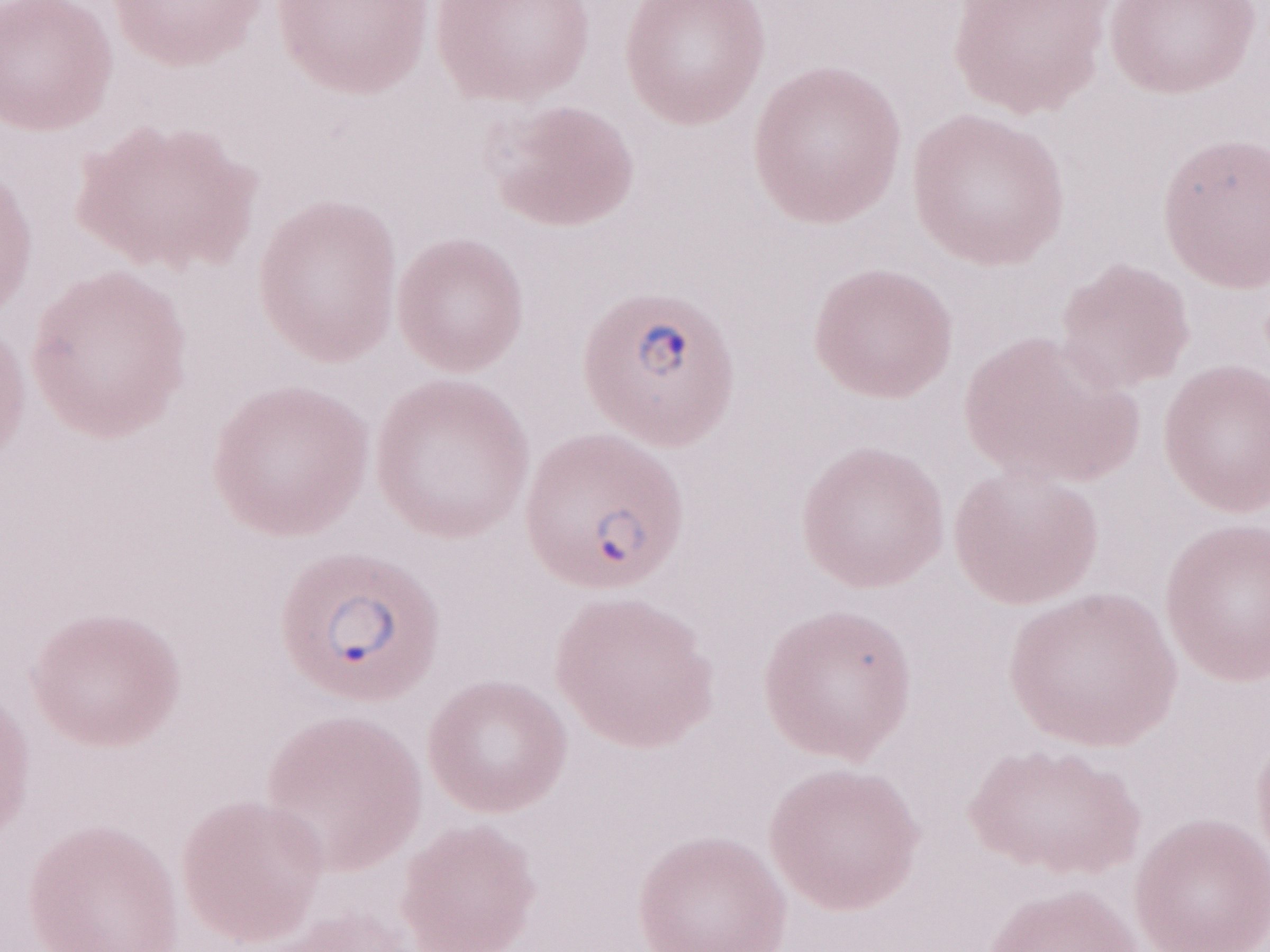 Image is 1270×952 pixels. 1,000x magnification. Thin blood smear. May-Grünwald-Giemsa-stained preparation. Olympus BX43 microscope, Olympus DP73 camera. Patient-level malaria diagnosis: positive. Single field of view.